Report the malaria status of this cell.
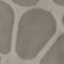
It is uninfected.

Giemsa-stained preparation. Thin blood smear. Acquired by smartphone through the microscope eyepiece. Automatically extracted cell patch, resized to 64 × 64 pixels.